Assess this cell for malaria.
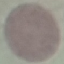
Uninfected.

image type = automatically extracted cell patch, resized to 64 × 64 pixels
stain = Giemsa
preparation = thin blood film
capture = smartphone camera at the microscope eyepiece